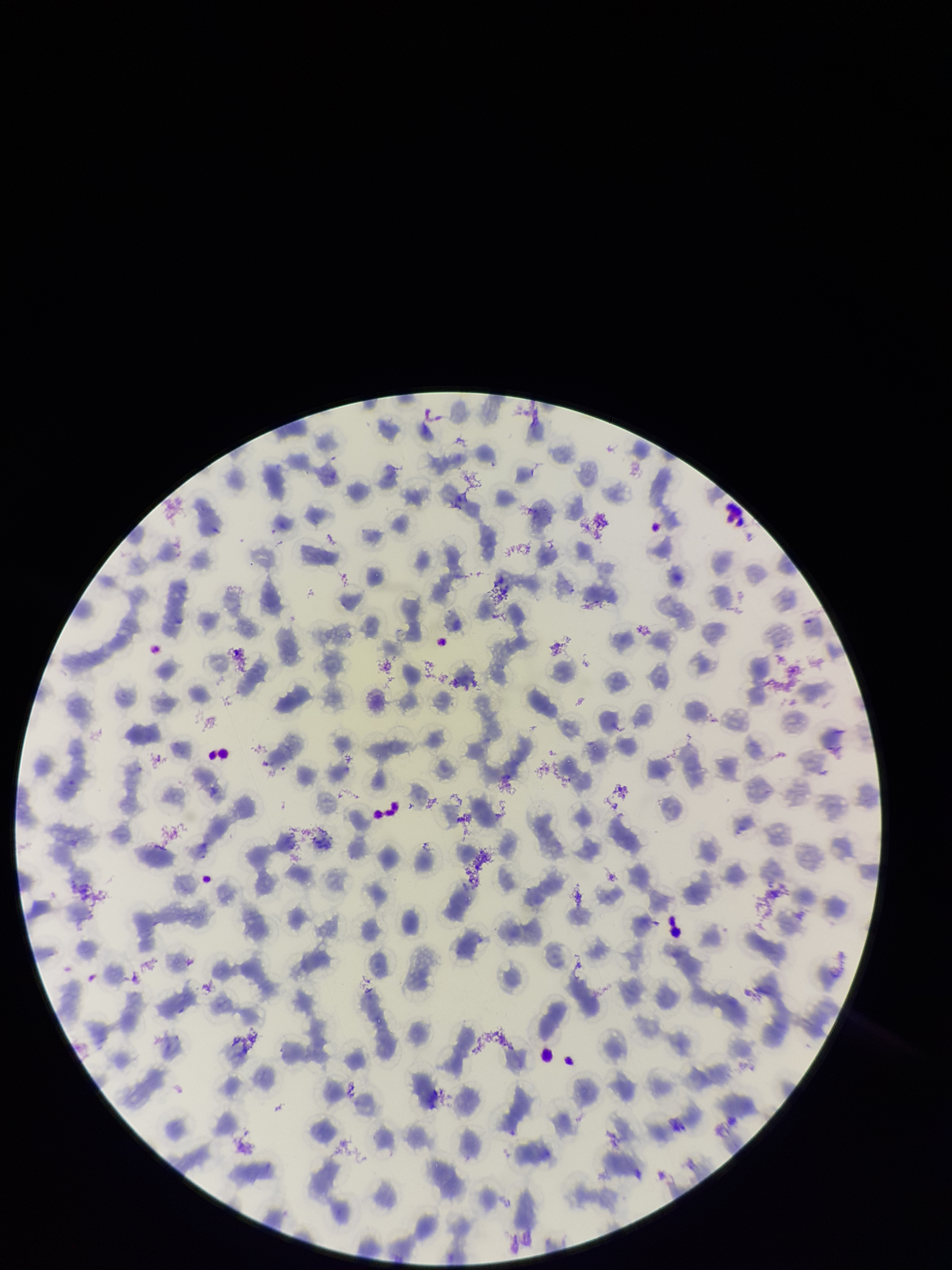

Parasitized red blood cells: none identified. Image is 952×1270 pixels. Smartphone photograph taken through the eyepiece of a microscope. Red blood cell count: 184. Species reported for this patient: Plasmodium falciparum. Preparation: thin smear. Giemsa stain. Parasitized red blood cell count: 0. One field from this slide. Patient malaria status: positive.